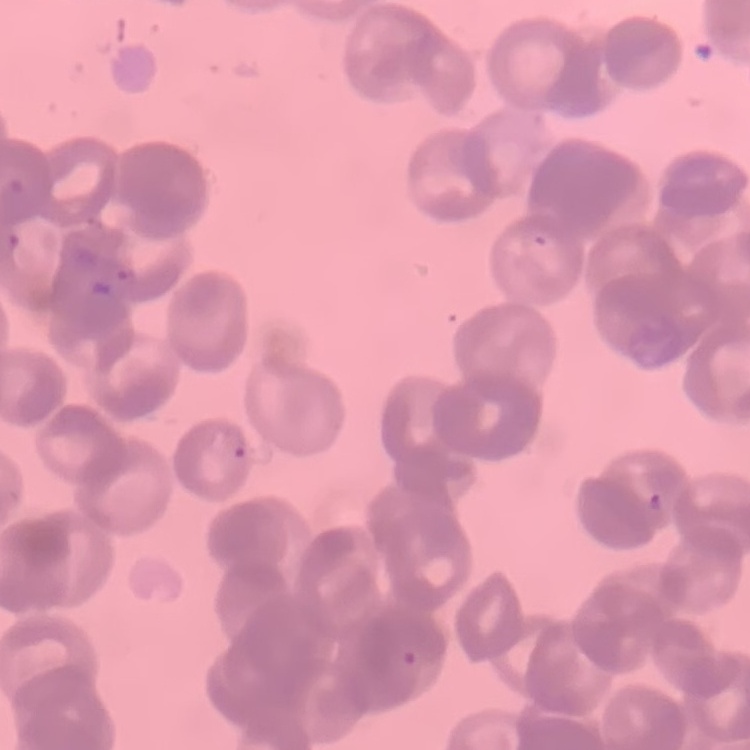

Summary:
  - Red blood cell morphology: rouleaux formation
  - Stain: Field's or Giemsa
  - Preparation: thin blood smear
  - Image type: one tile cut from a larger photomicrograph